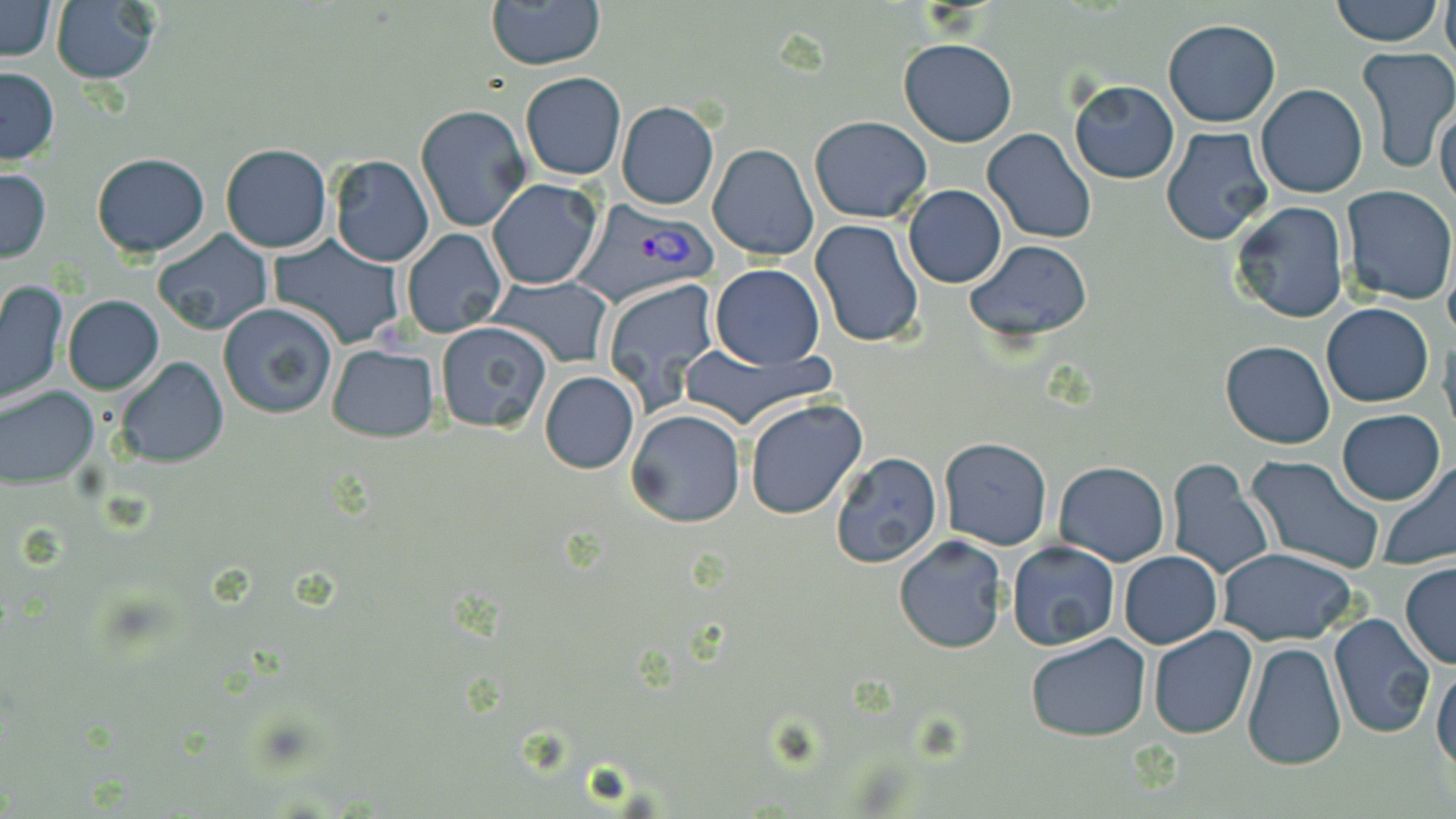
{
  "slide_level_diagnosis": "Plasmodium vivax",
  "magnification": "1000x",
  "uninfected_red_blood_cell_locations": "approximate bounding boxes as (x1, y1, x2, y2) in pixels: (0, 0, 59, 62), (51, 0, 160, 85), (486, 0, 604, 70), (1331, 0, 1444, 47), (1441, 0, 1456, 64), (1162, 20, 1282, 128), (898, 38, 1016, 147), (1354, 46, 1456, 172), (0, 66, 58, 163), (520, 72, 626, 180), (1068, 81, 1181, 183), (1257, 84, 1368, 198), (1436, 99, 1456, 213), (615, 102, 719, 210), (414, 103, 533, 234), (808, 115, 933, 222), (1161, 127, 1274, 245), (982, 128, 1100, 245), (707, 143, 817, 262), (220, 144, 332, 253), (90, 152, 211, 257), (329, 155, 435, 267), (0, 168, 50, 262), (487, 178, 603, 290), (902, 184, 1007, 288), (1340, 185, 1456, 305), (1229, 202, 1349, 323), (809, 220, 925, 350), (401, 229, 507, 339), (151, 231, 273, 337), (267, 235, 407, 350), (967, 238, 1095, 344), (710, 264, 824, 367), (489, 275, 613, 369), (601, 277, 720, 412), (0, 279, 68, 406), (62, 294, 164, 395), (219, 301, 338, 419), (1322, 303, 1435, 407), (436, 322, 552, 432), (1438, 334, 1456, 443), (1221, 340, 1334, 449), (675, 342, 838, 433), (327, 344, 440, 443), (116, 357, 229, 468), (539, 371, 639, 474), (0, 386, 99, 487), (744, 398, 868, 521), (1337, 408, 1445, 506), (626, 409, 746, 529), (937, 437, 1052, 550), (829, 452, 943, 568), (1243, 454, 1384, 572), (1166, 458, 1273, 578), (1379, 459, 1456, 567), (1054, 462, 1171, 566), (893, 536, 1008, 655), (1006, 543, 1122, 651), (1218, 547, 1359, 645), (1117, 550, 1222, 649), (1399, 562, 1456, 669), (1328, 614, 1436, 740), (1148, 624, 1258, 740), (1025, 633, 1150, 741), (1241, 640, 1349, 771), (1432, 658, 1456, 775)",
  "modality": "optical microscopy",
  "plasmodium_vivax_infected_red_blood_cell_locations": "approximate bounding boxes as (x1, y1, x2, y2) in pixels: (566, 196, 716, 311)",
  "stain": "May-Grünwald-Giemsa",
  "preparation": "thin blood film",
  "field_of_view": "one of a larger specimen",
  "image_size": "1456×819 pixels"
}